Report the malaria status of this cell.
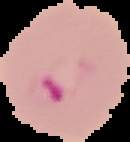
It is parasitized.

Summary:
  - Preparation: thin blood smear
  - Image type: segmented cell region with the area outside set to black
  - Image size: 130×142 pixels